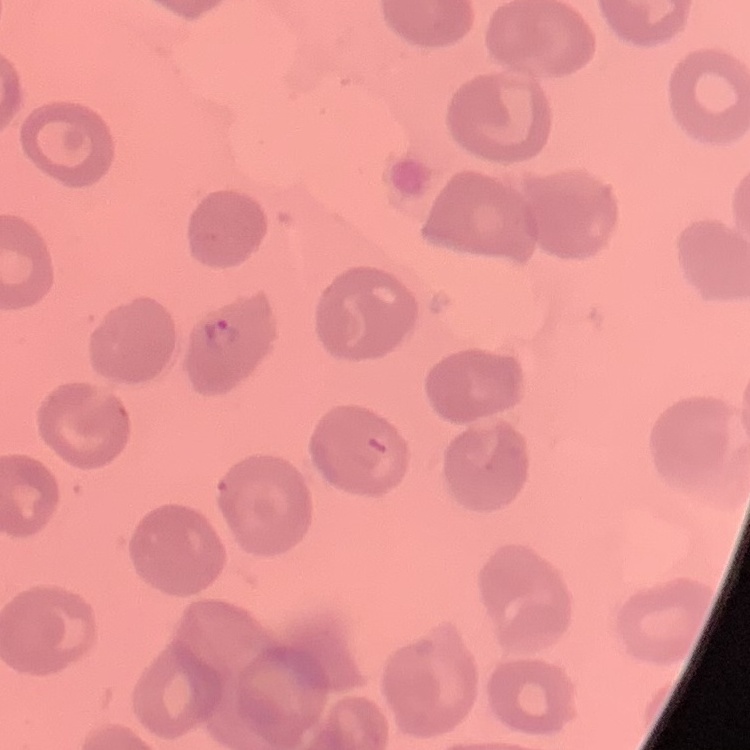

red blood cell morphology = no rouleaux formation
image type = one tile cut from a larger photomicrograph
preparation = thin blood smear
stain = Field's or Giemsa